Give the extent of all Plasmodium ovale-infected red blood cells.
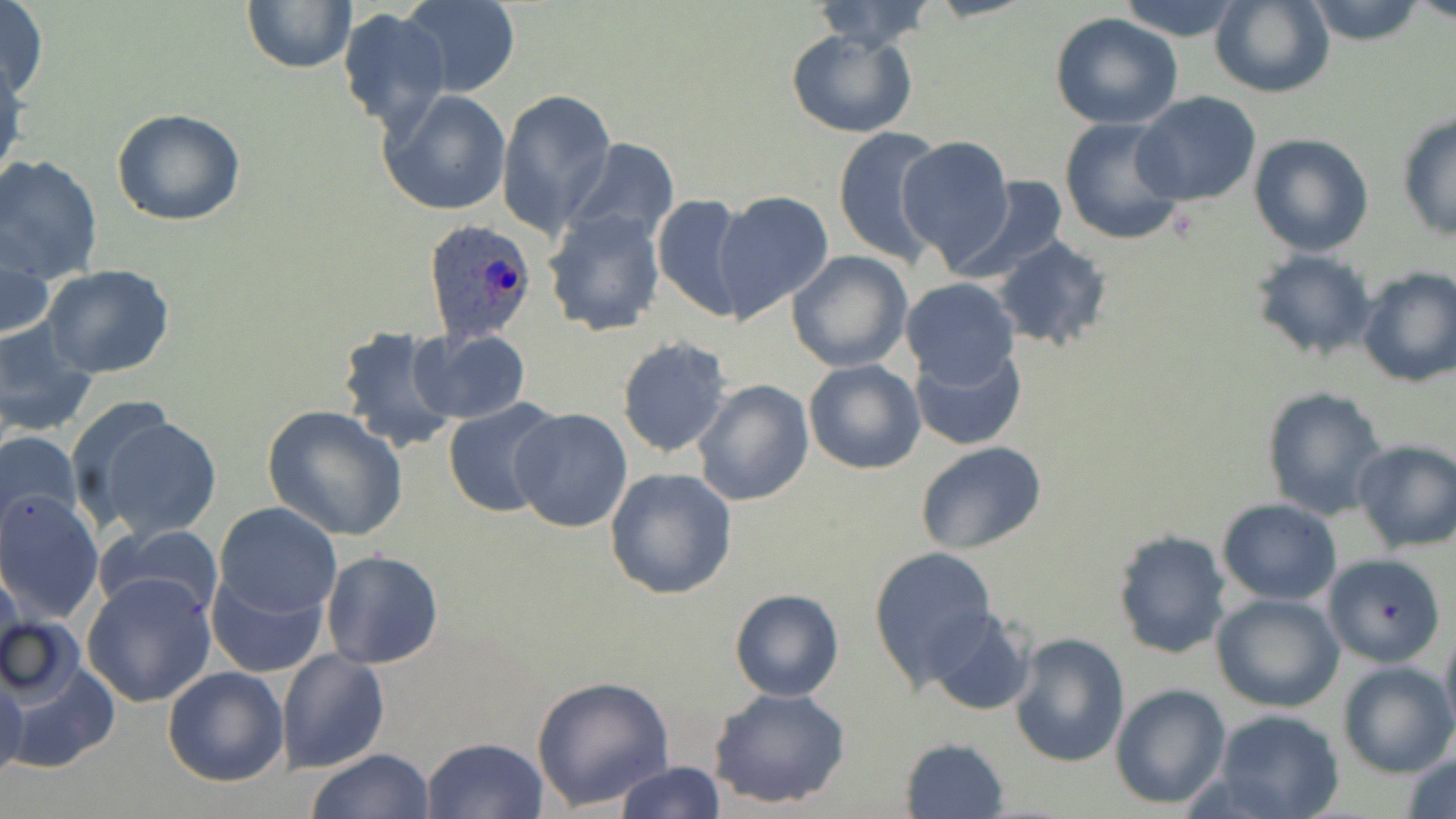
Approximate bounding boxes as [x1, y1, x2, y2] in pixels.
Plasmodium ovale-infected red blood cells: [423, 219, 538, 345].

slide-level diagnosis = Plasmodium ovale
preparation = thin blood film
modality = optical microscopy
image size = 1456×819 pixels
field of view = one of a larger specimen
stain = May-Grünwald-Giemsa
magnification = 1000x
uninfected red blood cell locations = approximate bounding boxes as [x1, y1, x2, y2] in pixels: [241, 0, 356, 74], [399, 0, 520, 98], [1113, 0, 1250, 41], [1209, 0, 1333, 98], [1301, 0, 1430, 45], [0, 1, 50, 103], [810, 1, 937, 51], [337, 8, 448, 132], [1050, 13, 1185, 129], [785, 27, 917, 137], [1, 58, 26, 189], [378, 88, 513, 215], [496, 89, 616, 236], [1131, 92, 1260, 207], [111, 108, 247, 227], [1395, 112, 1456, 242], [1057, 115, 1187, 245], [831, 127, 944, 262], [1248, 132, 1376, 257], [898, 136, 1014, 267], [568, 139, 680, 247], [0, 155, 103, 283], [950, 176, 1070, 281], [713, 191, 835, 322], [652, 193, 751, 322], [541, 208, 668, 338], [992, 236, 1112, 353], [1, 241, 52, 344], [788, 250, 912, 371], [1250, 250, 1378, 364], [1354, 264, 1456, 387], [41, 265, 175, 379], [900, 277, 1020, 387], [0, 317, 99, 437], [335, 324, 462, 457], [409, 327, 531, 424], [617, 337, 733, 457], [910, 343, 1026, 451], [803, 358, 925, 475], [692, 379, 815, 506], [1260, 385, 1390, 520], [442, 398, 566, 519], [261, 404, 409, 542], [509, 409, 635, 534], [84, 410, 224, 540], [0, 429, 83, 542], [1351, 438, 1456, 554], [914, 440, 1047, 555], [605, 466, 737, 599], [0, 492, 104, 622], [1218, 498, 1343, 603], [215, 502, 342, 620], [98, 523, 224, 623], [1112, 529, 1233, 660], [868, 546, 1000, 684], [321, 549, 444, 671], [1322, 554, 1446, 668], [0, 559, 26, 672], [207, 571, 328, 677], [83, 572, 219, 707], [729, 588, 843, 703], [1212, 593, 1345, 713], [923, 605, 1034, 715], [0, 614, 86, 709], [1439, 623, 1456, 742], [1006, 632, 1131, 768], [277, 646, 388, 773], [5, 659, 117, 775], [1336, 661, 1455, 779], [162, 666, 289, 787], [531, 674, 675, 812], [0, 677, 25, 779], [1111, 684, 1231, 809], [707, 688, 851, 807], [1212, 707, 1345, 819], [421, 737, 547, 819], [900, 737, 1011, 819], [1399, 747, 1456, 819], [306, 748, 436, 819], [613, 761, 724, 818]